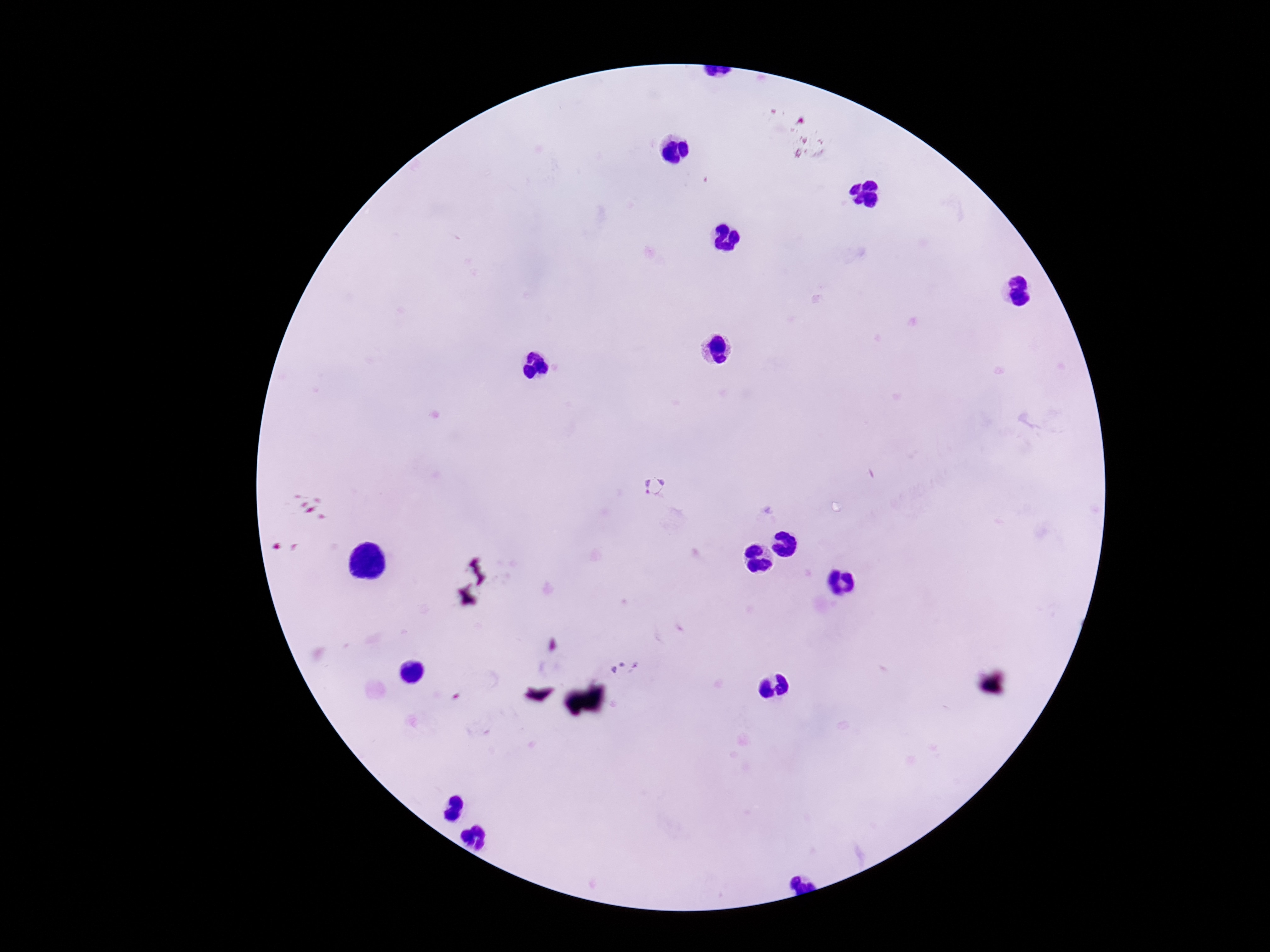
Plasmodium parasite locations = approximate centers as (x, y) in pixels: (655, 485), (625, 667)
magnification = 100x
field of view = single
image size = 1270×952 pixels
preparation = thick blood film
stain = Giemsa
patient malaria status = positive
capture = smartphone camera through the microscope eyepiece